State the preparation type.
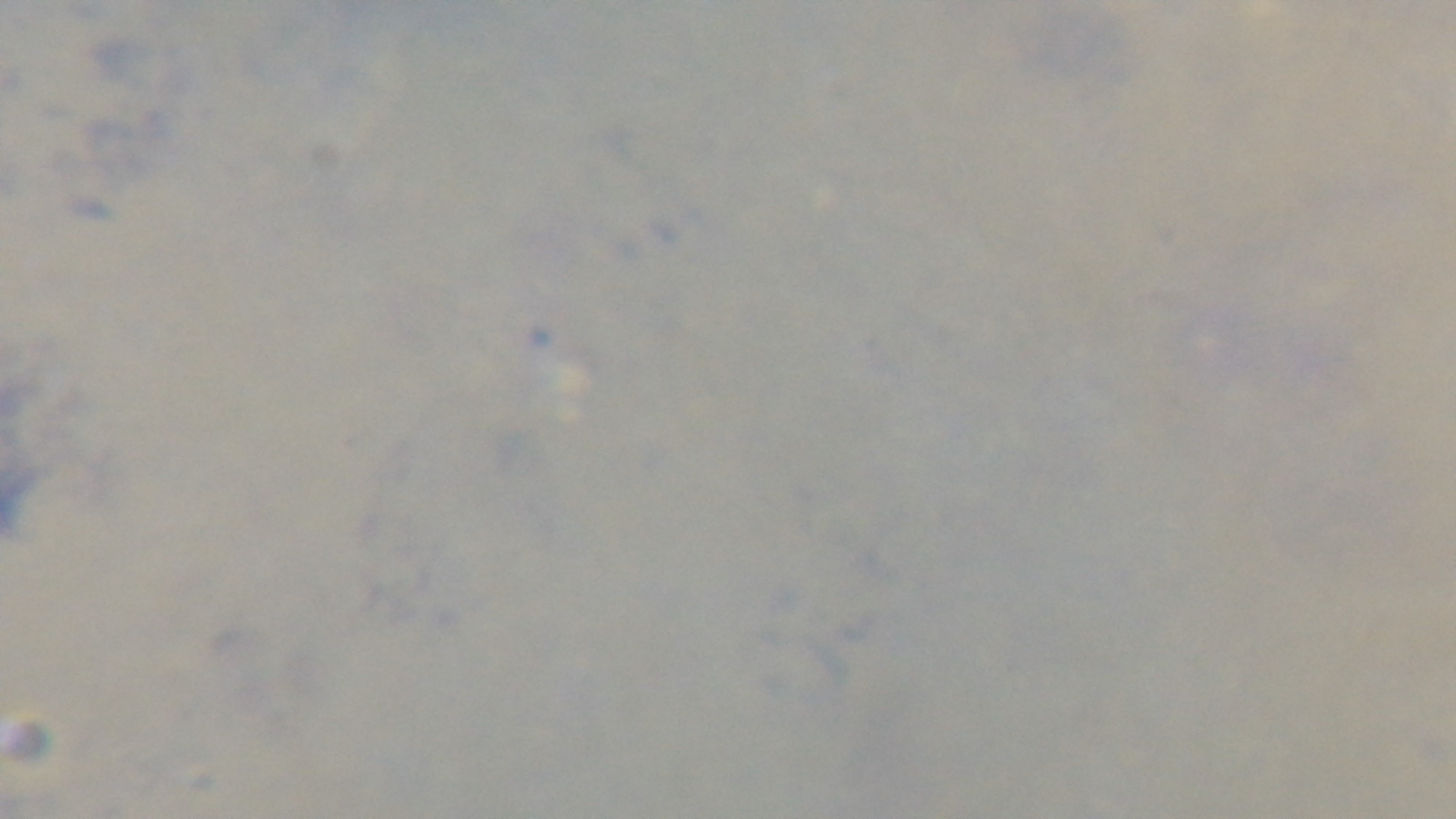

Thick.

stain: Giemsa
modality: light microscopy
capture: mounted 4K digital camera
objective: 100x oil immersion
field_of_view: single
malaria_status: negative